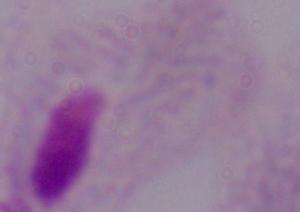
Captured at 1000x magnification. A trichomonad is seen. Photomicrograph.